Locate and identify every blood parasite.
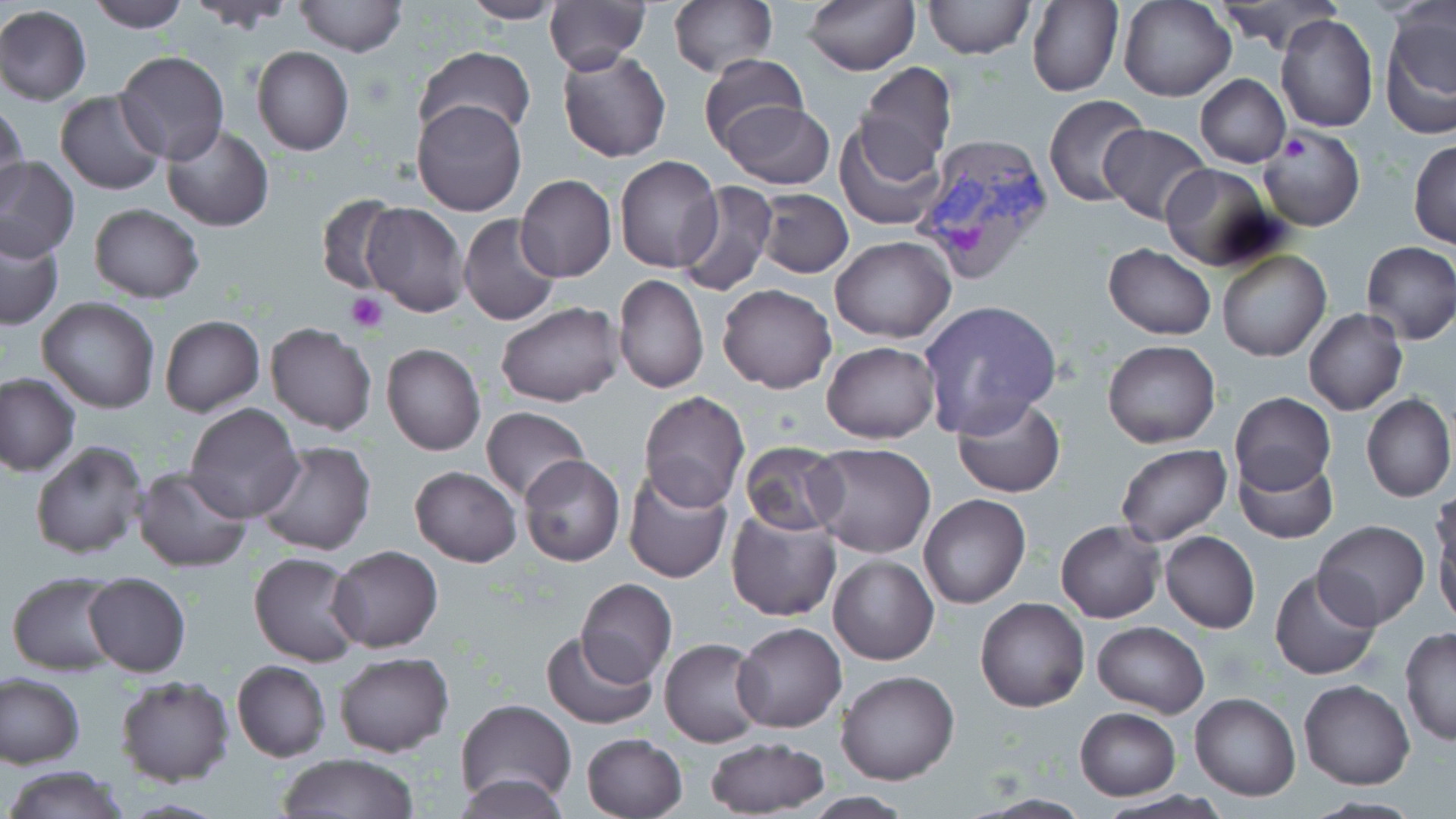
Approximate bounding boxes as (x1, y1, x2, y2) in pixels.
Plasmodium vivax-infected red blood cells: (909, 134, 1059, 287).
No Plasmodium falciparum, Plasmodium ovale, Plasmodium malariae, Babesia divergens, or Trypanosoma brucei observed.

slide_level_diagnosis: Plasmodium vivax
field_of_view: single
stain: May-Grünwald-Giemsa
preparation: thin blood smear
modality: optical microscopy
magnification: 1000x
uninfected_red_blood_cell_locations: 'approximate bounding boxes as (x1, y1, x2, y2) in pixels: (88, 0, 192, 31), (458, 0, 566, 24), (543, 0, 650, 73), (668, 0, 776, 79), (803, 0, 919, 75), (923, 0, 1033, 60), (1025, 0, 1123, 97), (190, 1, 293, 34), (292, 1, 408, 57), (1118, 1, 1237, 103), (1215, 2, 1345, 53), (0, 4, 93, 106), (1379, 9, 1456, 138), (1274, 12, 1378, 132), (252, 46, 354, 156), (412, 46, 537, 147), (557, 49, 670, 163), (115, 50, 229, 166), (696, 54, 810, 153), (856, 64, 958, 170), (1197, 74, 1290, 167), (53, 90, 168, 196), (1043, 94, 1150, 207), (412, 98, 527, 217), (0, 100, 31, 209), (720, 101, 834, 190), (835, 120, 944, 231), (1100, 123, 1210, 224), (161, 126, 274, 232), (1260, 127, 1364, 231), (1409, 140, 1455, 249), (1, 156, 79, 260), (614, 156, 723, 272), (1161, 164, 1278, 271), (514, 174, 617, 281), (675, 182, 778, 296), (754, 188, 853, 278), (317, 196, 405, 296), (359, 203, 470, 317), (88, 204, 204, 303), (457, 213, 562, 327), (1, 226, 65, 331), (831, 237, 956, 343), (1360, 240, 1456, 344), (1103, 244, 1216, 340), (1217, 248, 1329, 362), (613, 274, 709, 395), (717, 284, 836, 394), (36, 297, 161, 415), (918, 299, 1062, 437), (495, 302, 623, 407), (1304, 310, 1408, 415), (160, 315, 264, 416), (265, 322, 377, 435), (1102, 339, 1221, 449), (821, 342, 939, 445), (381, 343, 485, 456), (0, 372, 80, 476), (639, 391, 750, 510), (1230, 392, 1335, 495), (1361, 393, 1454, 503), (951, 394, 1066, 498), (184, 403, 304, 522), (480, 405, 590, 503), (257, 439, 377, 556), (29, 440, 149, 561), (740, 442, 848, 536), (805, 442, 937, 559), (1115, 444, 1232, 545), (1233, 450, 1339, 545), (518, 455, 626, 567), (410, 465, 521, 566), (133, 466, 254, 573), (621, 468, 734, 584), (918, 493, 1031, 609), (1430, 501, 1456, 625), (726, 508, 842, 621), (1056, 520, 1164, 623), (1313, 520, 1428, 630), (1160, 531, 1260, 633), (327, 545, 444, 652), (248, 551, 363, 667), (827, 554, 938, 665), (1269, 569, 1381, 681), (7, 570, 123, 674), (81, 571, 191, 677), (574, 579, 677, 686), (976, 598, 1088, 712), (1092, 621, 1209, 718), (733, 622, 846, 733), (542, 629, 657, 730), (1399, 629, 1456, 746), (660, 638, 768, 748), (335, 652, 453, 757), (230, 659, 331, 762), (836, 671, 959, 786), (1, 672, 86, 769), (115, 675, 234, 787), (1298, 679, 1415, 789), (1190, 691, 1300, 801), (456, 698, 576, 805), (1075, 707, 1180, 800), (581, 732, 687, 817), (704, 735, 831, 817), (278, 753, 420, 817), (4, 766, 133, 819), (458, 769, 572, 819), (1094, 791, 1230, 819), (972, 794, 1091, 817), (1304, 796, 1423, 818)'
platelet_locations: 'approximate bounding boxes as (x1, y1, x2, y2) in pixels: (1280, 133, 1315, 166), (345, 294, 386, 333)'
image_size: 1456×819 pixels